Locate and identify every blood parasite.
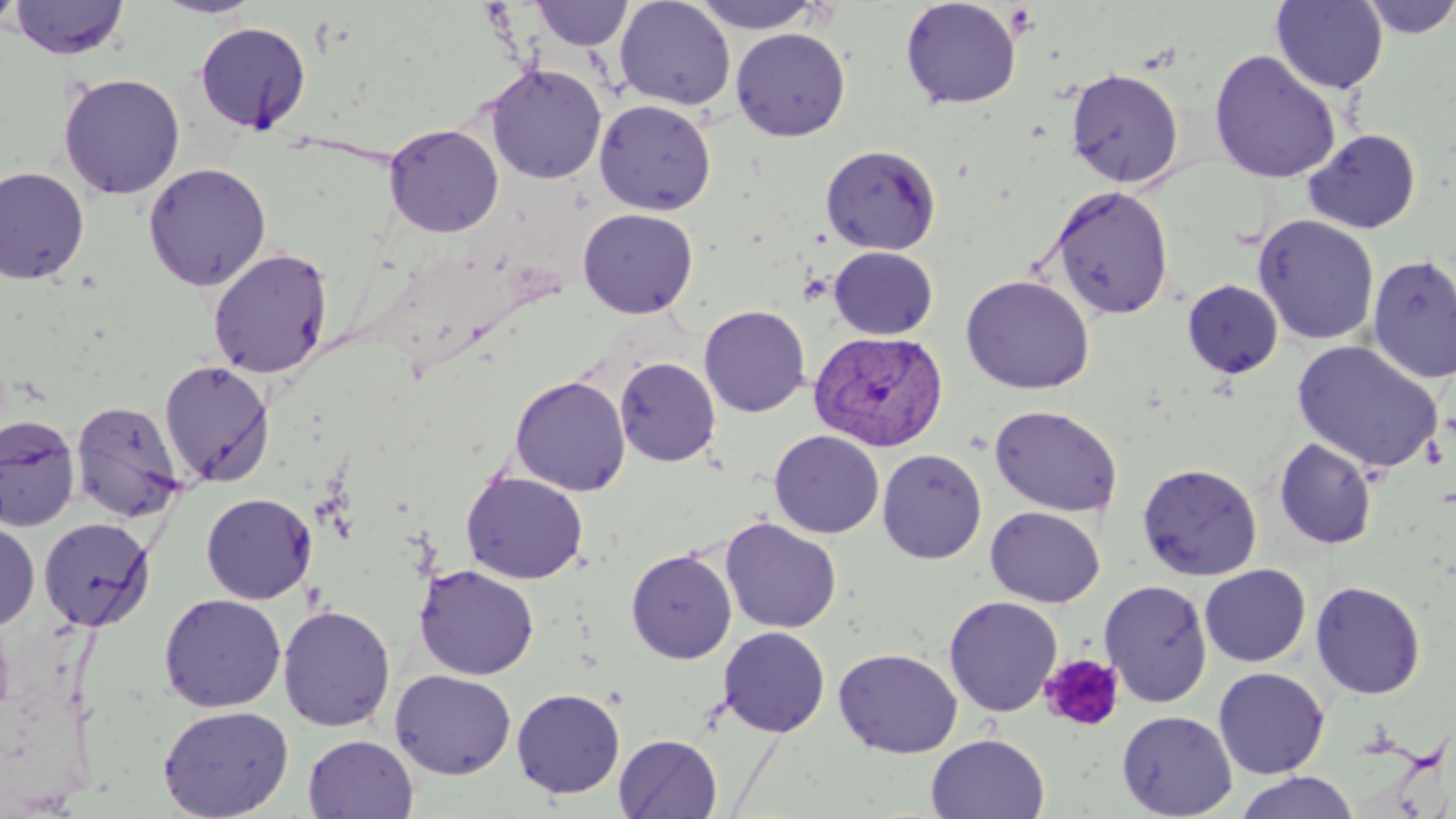
Approximate bounding boxes as named x1/y1/x2/y2 corners in pixels.
Plasmodium vivax-infected red blood cells: (x1=809, y1=330, x2=948, y2=452).
No Plasmodium falciparum, Plasmodium ovale, Plasmodium malariae, Babesia divergens, or Trypanosoma brucei observed.

slide_level_diagnosis: Plasmodium vivax
preparation: thin blood smear
image_size: 1456×819 pixels
platelet_locations: 'approximate bounding boxes as named x1/y1/x2/y2 corners in pixels: (x1=1039, y1=653, x2=1126, y2=732)'
uninfected_red_blood_cell_locations: 'approximate bounding boxes as named x1/y1/x2/y2 corners in pixels: (x1=0, y1=0, x2=24, y2=36), (x1=8, y1=0, x2=131, y2=60), (x1=151, y1=0, x2=267, y2=19), (x1=614, y1=0, x2=736, y2=111), (x1=900, y1=0, x2=1022, y2=109), (x1=1270, y1=0, x2=1389, y2=94), (x1=1356, y1=0, x2=1456, y2=39), (x1=530, y1=1, x2=634, y2=51), (x1=690, y1=1, x2=827, y2=33), (x1=194, y1=21, x2=311, y2=135), (x1=730, y1=27, x2=851, y2=142), (x1=1208, y1=50, x2=1342, y2=184), (x1=485, y1=63, x2=607, y2=184), (x1=1065, y1=68, x2=1184, y2=188), (x1=58, y1=72, x2=185, y2=200), (x1=594, y1=99, x2=717, y2=215), (x1=384, y1=123, x2=504, y2=237), (x1=1302, y1=128, x2=1421, y2=234), (x1=820, y1=144, x2=942, y2=255), (x1=142, y1=162, x2=272, y2=291), (x1=0, y1=166, x2=90, y2=285), (x1=1048, y1=184, x2=1175, y2=320), (x1=577, y1=208, x2=699, y2=318), (x1=1253, y1=214, x2=1380, y2=346), (x1=828, y1=246, x2=938, y2=340), (x1=207, y1=247, x2=333, y2=379), (x1=1366, y1=253, x2=1456, y2=384), (x1=961, y1=274, x2=1095, y2=395), (x1=1181, y1=279, x2=1284, y2=381), (x1=698, y1=304, x2=810, y2=417), (x1=1292, y1=340, x2=1444, y2=474), (x1=615, y1=357, x2=721, y2=467), (x1=159, y1=359, x2=276, y2=488), (x1=510, y1=375, x2=630, y2=495), (x1=71, y1=400, x2=186, y2=523), (x1=989, y1=404, x2=1123, y2=517), (x1=0, y1=414, x2=82, y2=532), (x1=769, y1=430, x2=884, y2=538), (x1=1274, y1=437, x2=1379, y2=550), (x1=877, y1=448, x2=988, y2=564), (x1=1137, y1=462, x2=1262, y2=581), (x1=461, y1=470, x2=589, y2=584), (x1=200, y1=492, x2=318, y2=604), (x1=985, y1=506, x2=1105, y2=607), (x1=38, y1=517, x2=155, y2=632), (x1=720, y1=517, x2=842, y2=633), (x1=0, y1=519, x2=40, y2=632), (x1=626, y1=548, x2=737, y2=663), (x1=414, y1=564, x2=540, y2=680), (x1=1199, y1=564, x2=1310, y2=667), (x1=1099, y1=579, x2=1212, y2=707), (x1=1311, y1=580, x2=1427, y2=699), (x1=158, y1=593, x2=287, y2=712), (x1=943, y1=596, x2=1063, y2=717), (x1=278, y1=604, x2=396, y2=731), (x1=718, y1=626, x2=830, y2=737), (x1=834, y1=647, x2=963, y2=758), (x1=1213, y1=667, x2=1330, y2=779), (x1=390, y1=669, x2=516, y2=780), (x1=511, y1=688, x2=625, y2=798), (x1=157, y1=705, x2=294, y2=819), (x1=1116, y1=710, x2=1237, y2=818), (x1=925, y1=733, x2=1050, y2=819), (x1=303, y1=734, x2=418, y2=818), (x1=613, y1=734, x2=723, y2=818), (x1=1233, y1=771, x2=1359, y2=819)'
magnification: 1000x
field_of_view: single
modality: optical microscopy
stain: May-Grünwald-Giemsa